Identify the parasite.
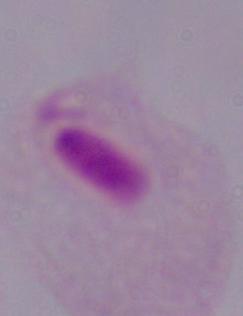
A trichomonad.

magnification: 1000x
modality: micrograph